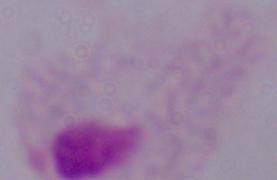
identification = trichomonad
modality = photomicrograph
magnification = 1000x